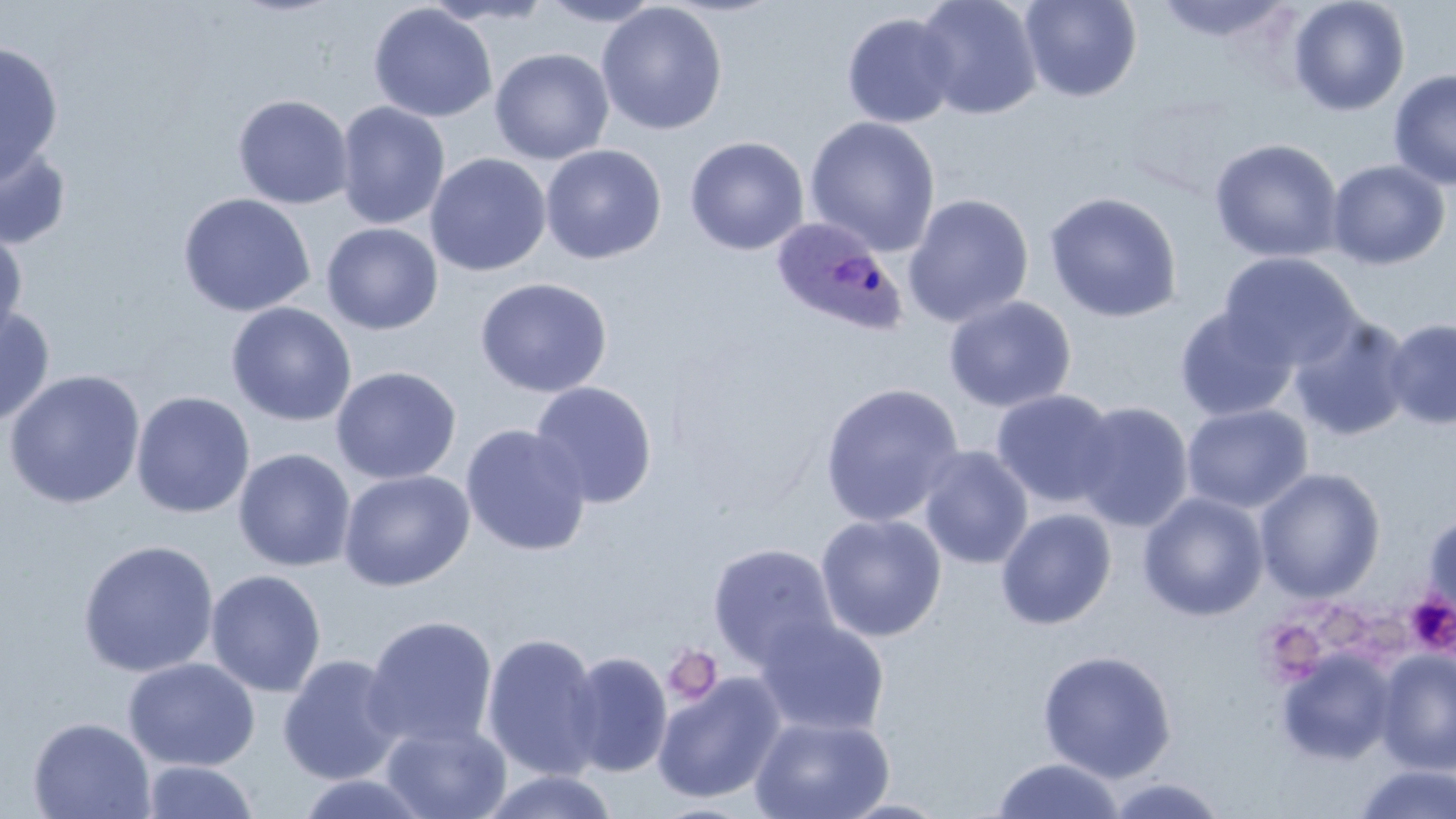
slide-level diagnosis = Plasmodium ovale
uninfected red blood cell locations = approximate bounding boxes as (x1,y1)-(x2,y2) corner pairs in pixels: (422,0)-(558,26), (538,0)-(666,27), (915,0)-(1043,119), (1020,0)-(1141,102), (1154,0)-(1295,43), (1288,0)-(1410,117), (596,2)-(728,136), (368,3)-(497,123), (841,12)-(959,129), (0,41)-(64,184), (490,48)-(614,165), (1388,68)-(1456,191), (232,94)-(354,209), (335,101)-(450,231), (804,116)-(941,256), (684,136)-(809,255), (1209,138)-(1344,263), (0,141)-(73,251), (540,144)-(666,264), (425,152)-(551,277), (1326,159)-(1452,271), (1044,191)-(1183,323), (177,192)-(315,318), (902,193)-(1034,327), (321,222)-(443,335), (0,226)-(28,349), (1218,253)-(1362,371), (475,277)-(613,398), (943,296)-(1077,413), (225,302)-(357,427), (0,303)-(56,429), (1174,305)-(1299,422), (1288,315)-(1414,442), (1382,317)-(1456,430), (330,366)-(462,485), (3,369)-(146,509), (530,381)-(658,509), (819,382)-(964,528), (990,388)-(1121,509), (131,390)-(255,518), (1072,401)-(1194,531), (1181,403)-(1312,514), (460,424)-(593,556), (918,445)-(1034,570), (233,448)-(356,572), (1255,467)-(1386,603), (338,469)-(475,592), (1137,492)-(1269,622), (995,507)-(1117,630), (1421,510)-(1456,620), (815,513)-(947,642), (77,539)-(219,678), (707,543)-(840,670), (205,569)-(327,697), (363,615)-(499,751), (754,616)-(890,737), (481,631)-(607,781), (1037,649)-(1177,782), (1275,649)-(1399,766), (1374,649)-(1456,775), (564,651)-(673,777), (277,654)-(405,785), (123,657)-(260,771), (652,672)-(787,804), (749,715)-(895,819), (27,716)-(156,819), (380,721)-(511,819), (990,757)-(1125,817), (141,760)-(259,819), (1353,763)-(1456,818), (478,770)-(619,819), (292,773)-(435,818), (1103,776)-(1230,819), (835,797)-(954,818)
field of view = single
image size = 1456×819 pixels
stain = May-Grünwald-Giemsa
preparation = thin blood film
modality = light microscopy
magnification = 1000x
platelet locations = approximate bounding boxes as (x1,y1)-(x2,y2) corner pairs in pixels: (1405,592)-(1456,656), (1322,609)-(1368,652), (1362,616)-(1412,660), (1256,618)-(1330,686), (663,645)-(723,706)
Plasmodium ovale-infected red blood cell locations = approximate bounding boxes as (x1,y1)-(x2,y2) corner pairs in pixels: (770,217)-(908,338)